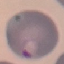

Summary:
  - Malaria status: parasitized
  - Stain: Giemsa
  - Preparation: thin blood smear
  - Capture: smartphone through the microscope eyepiece
  - Image type: cell patch, automatically extracted from a larger field of view and resized to 64 × 64 pixels